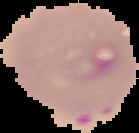
image type = segmented cell region on a black background
image size = 139×133 pixels
preparation = thin blood film
malaria status = parasitized